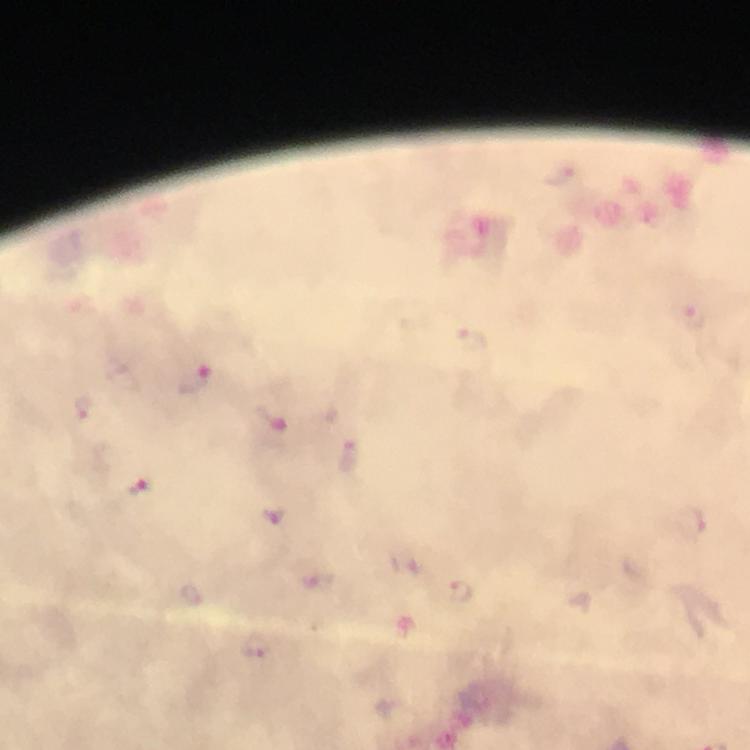
Approximate centers as [x, y] in pixels.
Summary:
  - Plasmodium parasite locations: [695, 318], [473, 339], [195, 382], [85, 406], [275, 419], [350, 460], [138, 488], [273, 515], [694, 522], [460, 590], [193, 594], [258, 647]
  - Stain: Giemsa
  - Image size: 750×750 pixels
  - Cropped from: a single field of view
  - Preparation: thick blood film
  - Magnification: 100x
  - Immersion oil: applied
  - Capture: smartphone photograph through a microscope
  - Context: from a malaria diagnostic workup